Assess this cell for malaria.
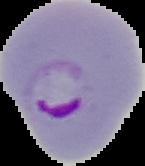

It is parasitized.

image size = 145×166 pixels
preparation = thin blood smear
image type = segmented cell region with the area outside set to black